Name the parasite shown.
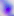
Toxoplasma gondii.

modality: photomicrograph
magnification: 400x